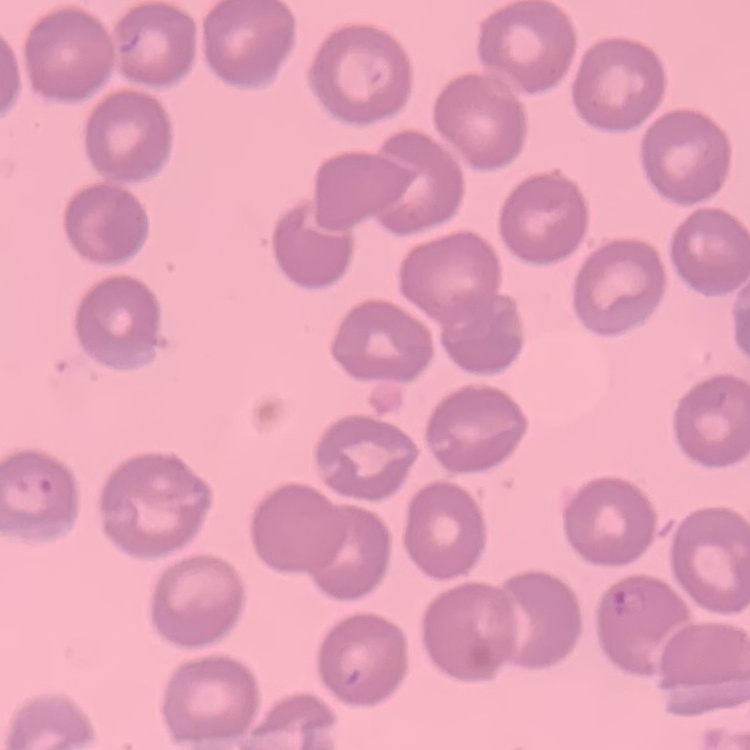

Summary:
  - Red blood cell morphology: no rouleaux formation
  - Preparation: thin blood film
  - Stain: Field's or Giemsa
  - Image type: square crop of a larger photomicrograph